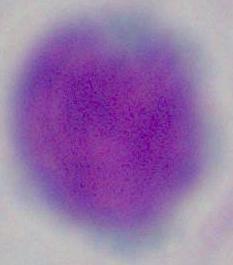 1000x magnification. A leukocyte is seen. Photomicrograph.